Outline each Plasmodium vivax-infected red blood cell.
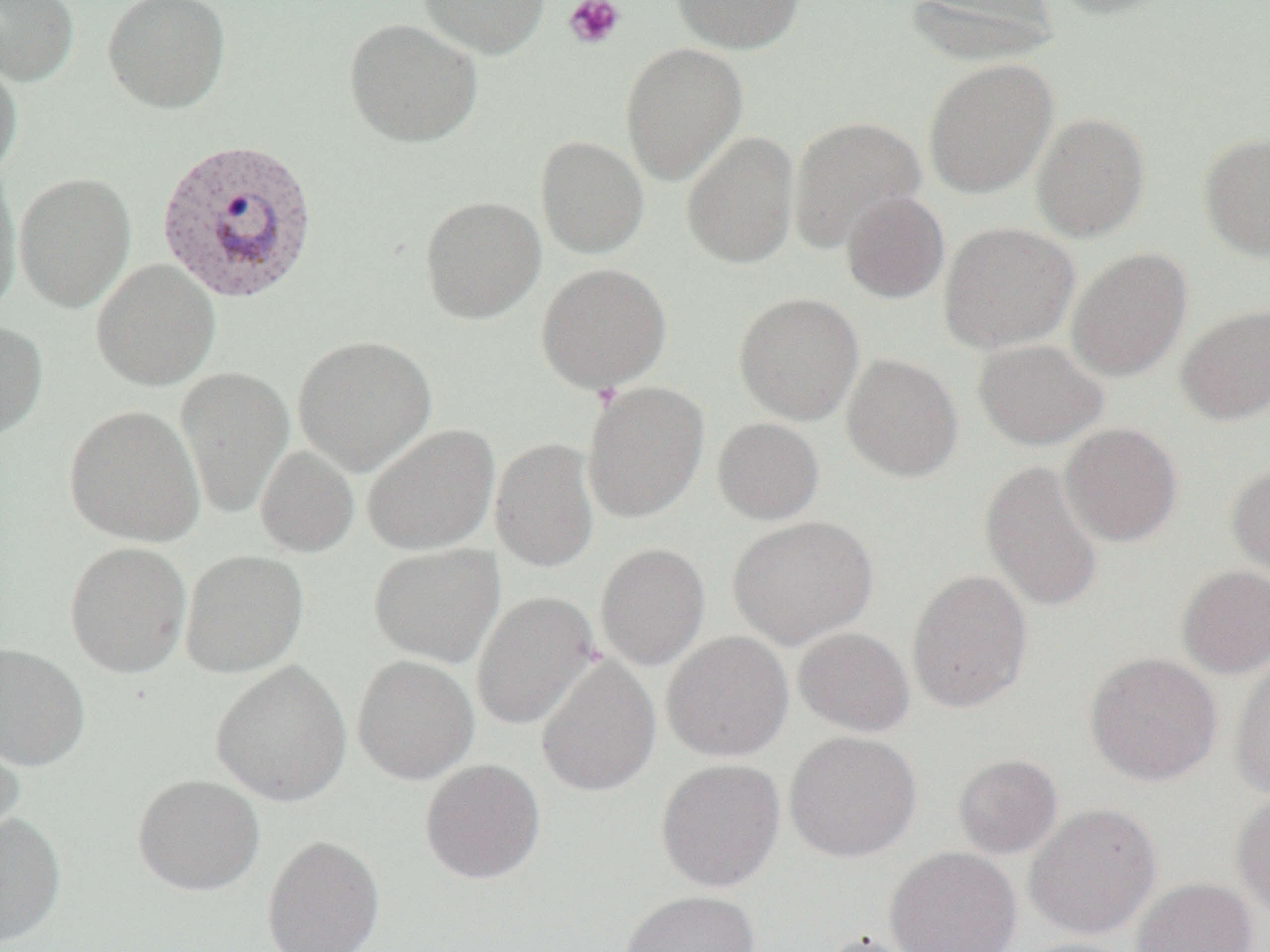

Approximate bounding boxes as named x1/y1/x2/y2 corners in pixels.
Plasmodium vivax-infected red blood cells: (x1=154, y1=138, x2=320, y2=304).

Summary:
  - Uninfected red blood cell locations: (x1=0, y1=0, x2=79, y2=86), (x1=102, y1=0, x2=231, y2=113), (x1=419, y1=0, x2=549, y2=59), (x1=672, y1=0, x2=804, y2=54), (x1=904, y1=0, x2=1058, y2=67), (x1=1047, y1=0, x2=1176, y2=20), (x1=344, y1=18, x2=482, y2=147), (x1=620, y1=42, x2=748, y2=186), (x1=0, y1=57, x2=23, y2=180), (x1=922, y1=58, x2=1058, y2=199), (x1=1030, y1=112, x2=1151, y2=242), (x1=787, y1=115, x2=926, y2=253), (x1=681, y1=130, x2=800, y2=269), (x1=1198, y1=133, x2=1270, y2=261), (x1=535, y1=135, x2=649, y2=258), (x1=0, y1=165, x2=22, y2=315), (x1=15, y1=171, x2=136, y2=313), (x1=841, y1=192, x2=949, y2=303), (x1=420, y1=195, x2=546, y2=324), (x1=938, y1=221, x2=1080, y2=354), (x1=1066, y1=248, x2=1192, y2=382), (x1=91, y1=258, x2=221, y2=391), (x1=535, y1=262, x2=673, y2=393), (x1=733, y1=292, x2=864, y2=426), (x1=1176, y1=304, x2=1270, y2=425), (x1=0, y1=320, x2=48, y2=440), (x1=292, y1=334, x2=437, y2=476), (x1=973, y1=338, x2=1108, y2=450), (x1=842, y1=353, x2=963, y2=482), (x1=175, y1=365, x2=294, y2=519), (x1=581, y1=382, x2=709, y2=522), (x1=63, y1=405, x2=206, y2=547), (x1=712, y1=417, x2=825, y2=525), (x1=361, y1=423, x2=500, y2=556), (x1=1060, y1=423, x2=1183, y2=547), (x1=491, y1=437, x2=600, y2=572), (x1=254, y1=445, x2=360, y2=558), (x1=979, y1=459, x2=1104, y2=613), (x1=1226, y1=461, x2=1270, y2=585), (x1=727, y1=516, x2=878, y2=649), (x1=64, y1=541, x2=191, y2=678), (x1=595, y1=542, x2=711, y2=671), (x1=369, y1=544, x2=504, y2=667), (x1=180, y1=550, x2=308, y2=678), (x1=1177, y1=565, x2=1270, y2=679), (x1=906, y1=569, x2=1033, y2=713), (x1=471, y1=591, x2=600, y2=730), (x1=793, y1=626, x2=914, y2=736), (x1=661, y1=631, x2=794, y2=762), (x1=0, y1=642, x2=91, y2=770), (x1=1085, y1=652, x2=1222, y2=786), (x1=1230, y1=652, x2=1270, y2=800), (x1=352, y1=655, x2=479, y2=784), (x1=535, y1=655, x2=661, y2=797), (x1=210, y1=660, x2=353, y2=807), (x1=0, y1=726, x2=24, y2=843), (x1=785, y1=730, x2=921, y2=862), (x1=953, y1=754, x2=1063, y2=858), (x1=419, y1=758, x2=546, y2=885), (x1=655, y1=758, x2=785, y2=892), (x1=133, y1=774, x2=265, y2=896), (x1=1232, y1=790, x2=1270, y2=922), (x1=1024, y1=803, x2=1161, y2=939), (x1=0, y1=812, x2=66, y2=948), (x1=261, y1=834, x2=385, y2=952), (x1=885, y1=847, x2=1022, y2=952), (x1=1131, y1=877, x2=1258, y2=952), (x1=617, y1=889, x2=761, y2=952), (x1=817, y1=931, x2=923, y2=952), (x1=1010, y1=938, x2=1140, y2=952)
  - Platelet locations: (x1=564, y1=0, x2=625, y2=49), (x1=591, y1=381, x2=623, y2=410)
  - Slide-level diagnosis: Plasmodium vivax
  - Modality: light microscopy
  - Magnification: 1000x
  - Image size: 1270×952 pixels
  - Field of view: one of a larger specimen
  - Preparation: thin blood film